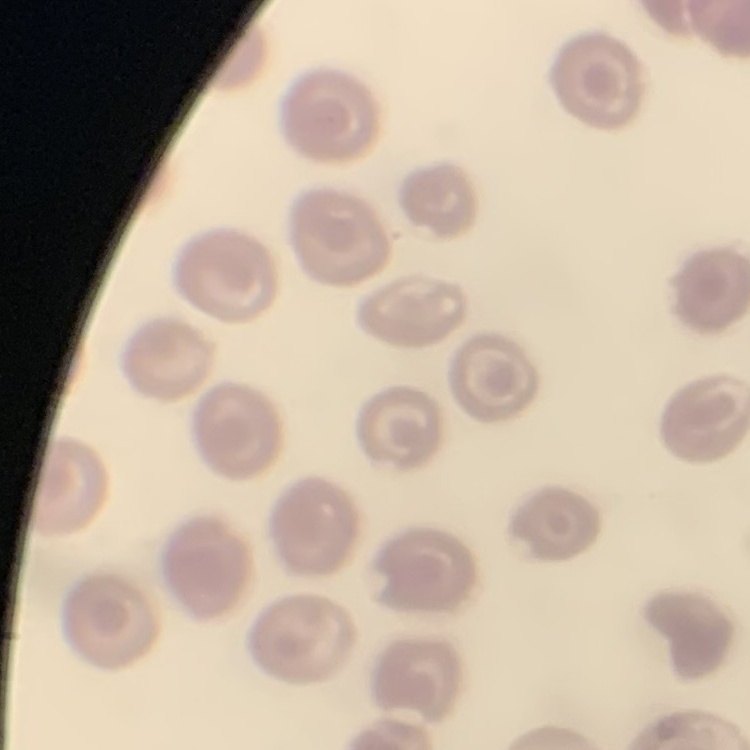

Summary:
  - Erythrocyte morphology: no rouleaux formation
  - Preparation: thin peripheral smear
  - Image type: one tile cut from a larger photomicrograph
  - Stain: Field's or Giemsa